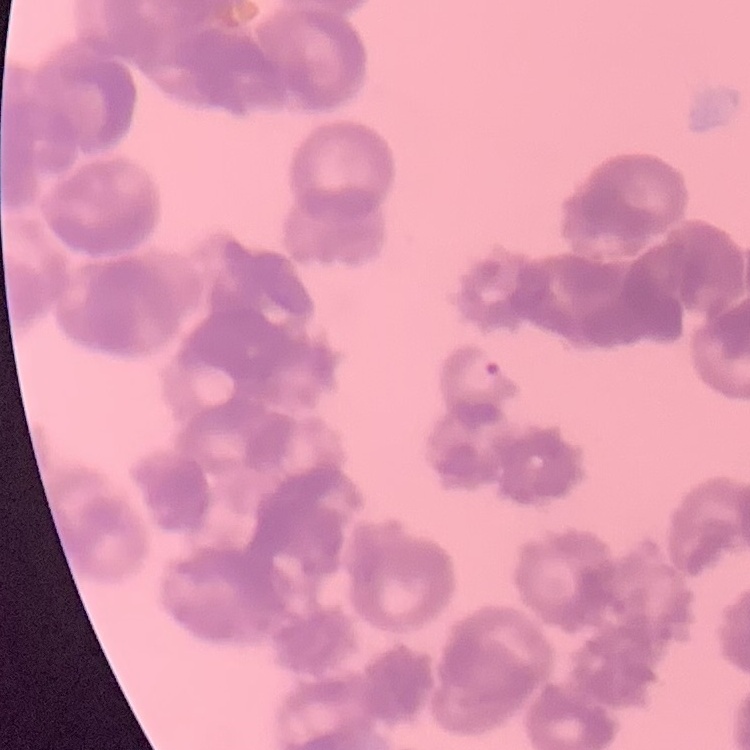

Summary:
  - Erythrocyte morphology: rouleaux formation
  - Preparation: thin blood smear
  - Stain: Field's or Giemsa
  - Image type: one tile cut from a larger photomicrograph